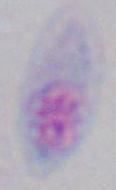

modality = photomicrograph
magnification = 1000x
identification = Toxoplasma gondii